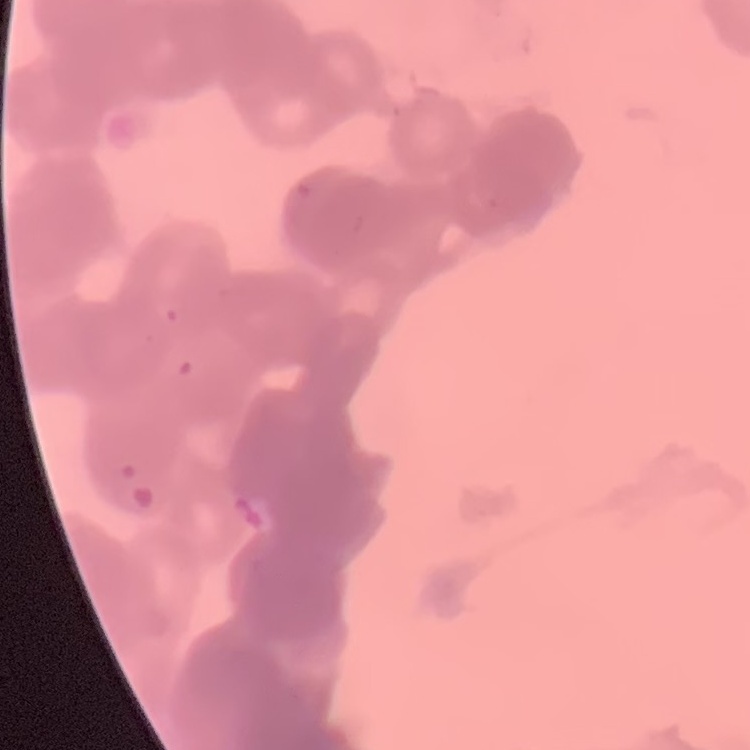

The red blood cells exhibit rouleaux formation. Stained with either Field's or Giemsa. One tile cut from a larger photomicrograph. Thin blood film.